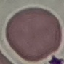
result = negative for malaria parasites
preparation = thin blood smear
capture = smartphone through the microscope eyepiece
image type = automatically extracted cell patch, resized to 64 × 64 pixels
stain = Giemsa